Identify the blood parasite species.
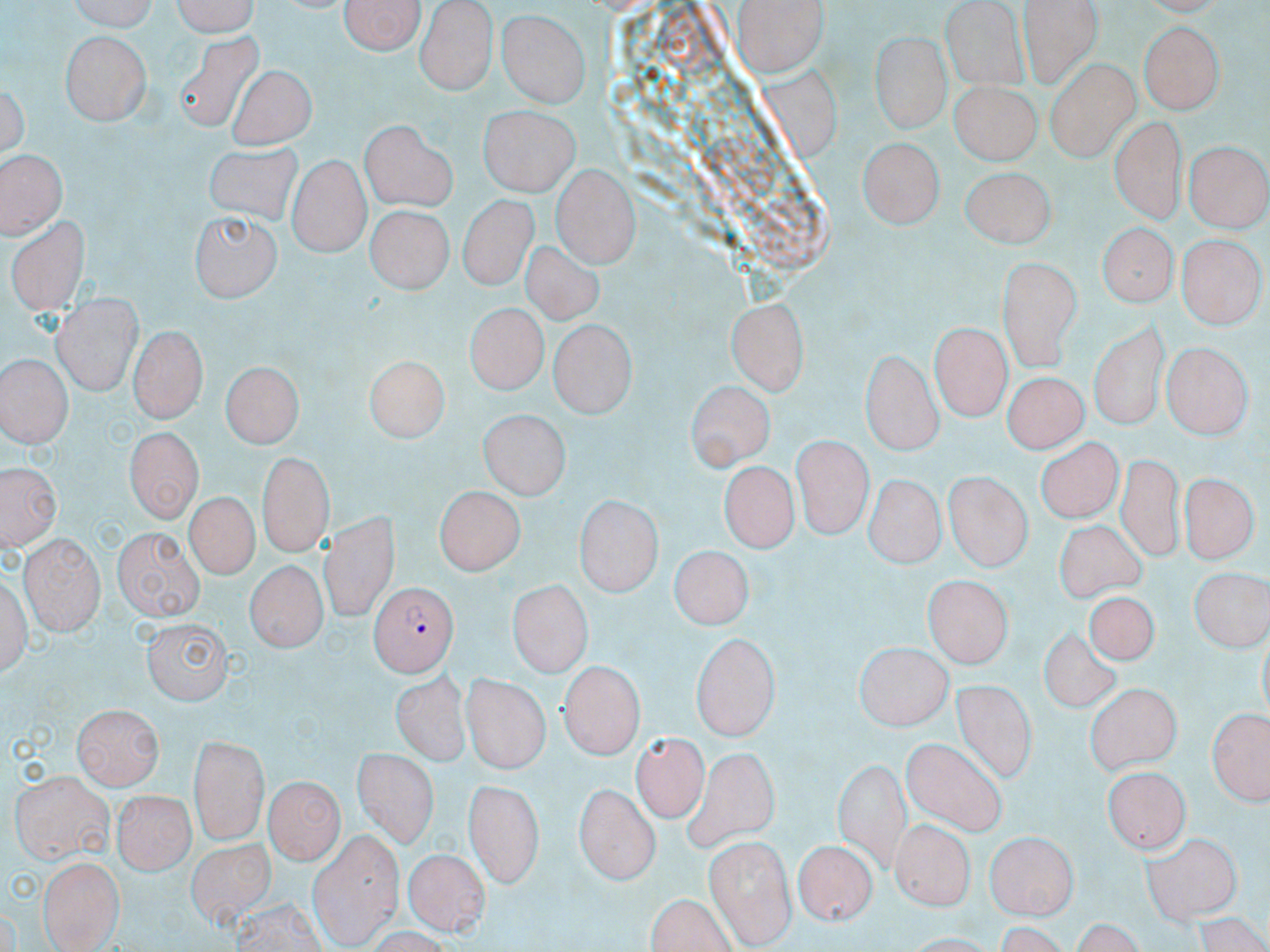

Plasmodium falciparum.

stain = May-Grünwald-Giemsa
preparation = thin blood film
Plasmodium falciparum-infected red blood cell locations = approximate bounding boxes as [x1, y1, x2, y2] in pixels: [368, 580, 458, 677]
field of view = single
modality = optical microscopy
magnification = 1000x
uninfected red blood cell locations = approximate bounding boxes as [x1, y1, x2, y2] in pixels: [70, 0, 161, 34], [166, 0, 259, 35], [341, 0, 425, 58], [414, 0, 498, 94], [1022, 0, 1100, 85], [736, 2, 828, 78], [496, 9, 592, 109], [1138, 22, 1224, 111], [491, 29, 585, 179], [868, 31, 951, 132], [178, 32, 262, 136], [62, 33, 149, 126], [1046, 60, 1136, 161], [757, 62, 844, 158], [231, 66, 313, 149], [950, 80, 1036, 167], [478, 107, 579, 195], [1111, 116, 1184, 225], [360, 118, 457, 211], [1119, 130, 1247, 228], [859, 140, 942, 231], [1187, 140, 1268, 230], [204, 144, 305, 226], [0, 151, 68, 235], [288, 154, 367, 256], [552, 166, 639, 267], [961, 166, 1054, 248], [455, 194, 537, 291], [363, 203, 451, 295], [187, 209, 280, 301], [9, 218, 88, 315], [1097, 224, 1174, 309], [1180, 236, 1261, 327], [524, 242, 600, 325], [996, 255, 1082, 372], [50, 293, 141, 396], [725, 295, 811, 397], [463, 301, 549, 391], [932, 321, 1010, 422], [547, 322, 635, 418], [1087, 322, 1169, 430], [129, 328, 205, 422], [1162, 340, 1251, 437], [862, 350, 943, 452], [2, 354, 73, 447], [361, 356, 448, 443], [219, 361, 300, 451], [1001, 374, 1093, 453], [686, 383, 772, 472], [481, 412, 567, 499], [121, 425, 203, 524], [792, 436, 868, 542], [1038, 438, 1122, 524], [255, 453, 335, 554], [1116, 454, 1189, 558], [3, 460, 59, 554], [719, 464, 802, 549], [946, 472, 1031, 575], [1185, 473, 1253, 563], [869, 478, 941, 566], [437, 485, 529, 572], [185, 489, 258, 577], [578, 495, 661, 597], [323, 510, 400, 619], [1052, 521, 1145, 600], [114, 526, 204, 619], [19, 537, 104, 633], [668, 547, 755, 631], [247, 559, 326, 658], [1188, 569, 1268, 651], [3, 570, 35, 685], [924, 579, 1011, 667], [509, 581, 592, 677], [1087, 595, 1156, 666], [141, 617, 233, 704], [1041, 625, 1124, 717], [690, 634, 779, 739], [856, 645, 953, 733], [558, 661, 646, 758], [461, 669, 549, 773], [391, 672, 469, 764], [947, 677, 1041, 783], [1086, 685, 1180, 774], [71, 705, 162, 791], [1210, 705, 1270, 804], [631, 734, 709, 822], [187, 736, 267, 844], [901, 739, 1004, 836], [681, 748, 779, 849], [353, 749, 437, 848], [834, 759, 913, 867], [13, 769, 114, 862], [1102, 769, 1190, 857], [267, 776, 342, 860], [464, 781, 542, 888], [576, 783, 660, 883], [113, 791, 192, 874], [890, 822, 971, 914], [982, 824, 1076, 917], [1139, 831, 1244, 922], [307, 832, 400, 950], [706, 835, 795, 944], [192, 836, 274, 922], [795, 840, 875, 927], [403, 849, 490, 934], [38, 856, 125, 948], [644, 896, 739, 952]
image size = 1270×952 pixels